Outline each blood parasite and name the species.
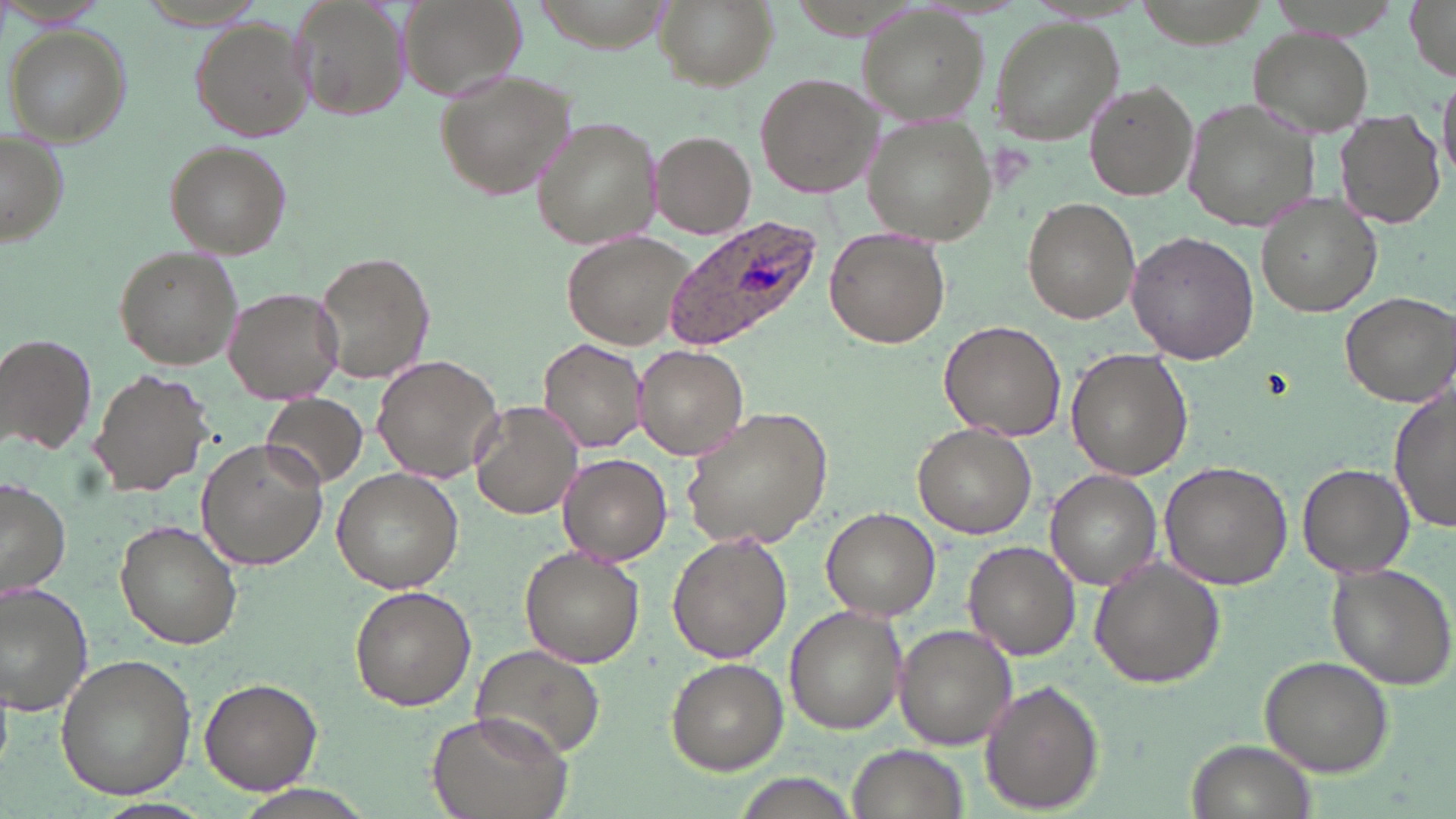

Approximate bounding boxes as [x1, y1, x2, y2] in pixels.
Plasmodium ovale-infected red blood cells: [658, 218, 824, 352].
No Plasmodium falciparum, Plasmodium malariae, Plasmodium vivax, Babesia divergens, or Trypanosoma brucei observed.

slide-level diagnosis = Plasmodium ovale
stain = May-Grünwald-Giemsa
modality = optical microscopy
magnification = 1000x
field of view = single
image size = 1456×819 pixels
preparation = thin blood film
uninfected red blood cell locations = approximate bounding boxes as [x1, y1, x2, y2] in pixels: [293, 0, 412, 118], [398, 0, 528, 105], [655, 0, 774, 91], [1403, 0, 1456, 81], [856, 7, 992, 126], [989, 18, 1124, 142], [189, 19, 312, 141], [6, 25, 130, 145], [1247, 27, 1374, 136], [433, 69, 577, 200], [754, 71, 881, 196], [1438, 74, 1456, 186], [1085, 81, 1199, 202], [1181, 96, 1323, 232], [1335, 109, 1446, 229], [531, 115, 664, 253], [863, 117, 1000, 245], [1, 129, 70, 248], [651, 130, 757, 239], [164, 140, 293, 259], [1256, 192, 1384, 317], [1024, 198, 1139, 323], [825, 225, 948, 349], [563, 230, 700, 351], [1127, 230, 1261, 363], [112, 245, 243, 371], [313, 249, 437, 387], [222, 287, 345, 406], [1338, 289, 1456, 407], [940, 320, 1068, 440], [1, 333, 97, 454], [538, 338, 646, 454], [633, 344, 749, 461], [1067, 348, 1193, 479], [371, 354, 505, 483], [89, 368, 213, 498], [1390, 382, 1456, 536], [260, 393, 368, 489], [469, 399, 584, 520], [679, 405, 835, 550], [913, 423, 1038, 539], [196, 439, 329, 573], [557, 453, 671, 565], [1158, 461, 1293, 590], [1297, 463, 1413, 581], [331, 467, 463, 593], [1046, 470, 1161, 587], [0, 478, 71, 600], [821, 508, 940, 619], [114, 519, 243, 649], [667, 533, 793, 662], [962, 541, 1082, 660], [520, 547, 645, 667], [1088, 557, 1226, 688], [1325, 563, 1456, 691], [0, 581, 97, 718], [349, 586, 477, 709], [783, 607, 907, 735], [894, 624, 1017, 752], [470, 645, 604, 760], [54, 653, 196, 803], [1260, 656, 1393, 776], [666, 657, 789, 773], [198, 678, 322, 796], [979, 682, 1104, 812], [426, 709, 574, 819], [1190, 738, 1312, 818], [847, 743, 974, 819], [235, 786, 376, 819], [94, 799, 216, 819]